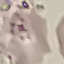
malaria status = uninfected
preparation = thin blood film
stain = Giemsa
image type = automatically extracted cell patch, resized to 64 × 64 pixels
capture = smartphone camera at the microscope eyepiece